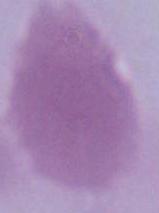
Summary:
  - Identification: erythrocyte
  - Magnification: 1000x
  - Modality: micrograph